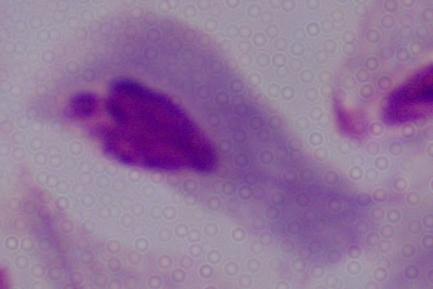

Photomicrograph. A trichomonad is shown. 1000x magnification.